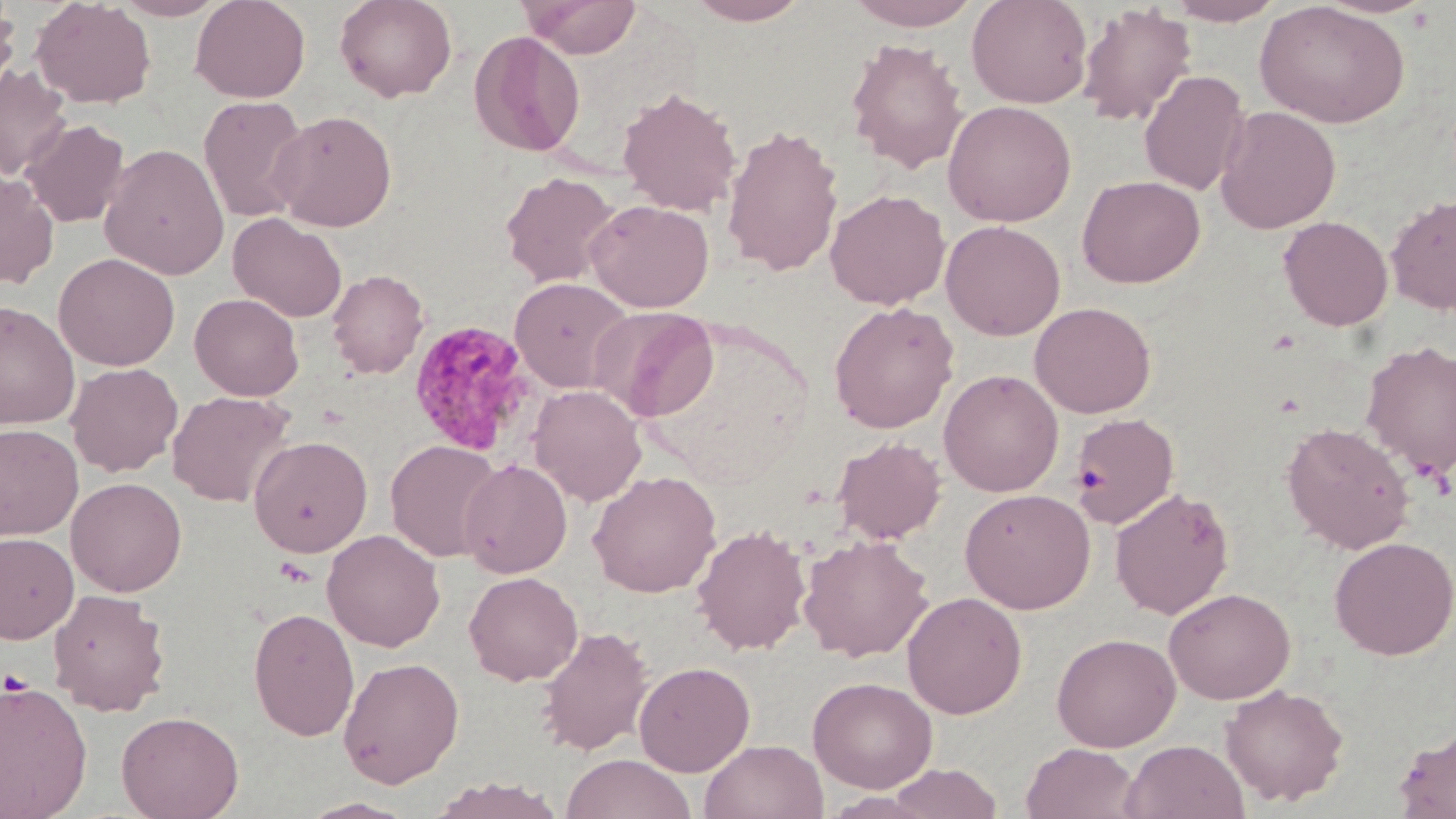
slide_level_diagnosis: Plasmodium malariae
field_of_view: single
platelet_locations: 'approximate bounding boxes as named x1/y1/x2/y2 corners in pixels: (x1=2, y1=668, x2=32, y2=696)'
plasmodium_malariae_infected_red_blood_cell_locations: 'approximate bounding boxes as named x1/y1/x2/y2 corners in pixels: (x1=408, y1=320, x2=534, y2=456)'
stain: May-Grünwald-Giemsa
magnification: 1000x
preparation: thin blood smear
image_size: 1456×819 pixels
modality: light microscopy
uninfected_red_blood_cell_locations: 'approximate bounding boxes as named x1/y1/x2/y2 corners in pixels: (x1=31, y1=0, x2=156, y2=109), (x1=114, y1=0, x2=227, y2=21), (x1=191, y1=0, x2=310, y2=102), (x1=334, y1=0, x2=457, y2=102), (x1=519, y1=0, x2=642, y2=58), (x1=684, y1=0, x2=814, y2=25), (x1=844, y1=0, x2=982, y2=30), (x1=966, y1=0, x2=1093, y2=109), (x1=1163, y1=0, x2=1286, y2=26), (x1=0, y1=2, x2=20, y2=103), (x1=1255, y1=2, x2=1411, y2=129), (x1=1075, y1=3, x2=1197, y2=127), (x1=469, y1=30, x2=586, y2=157), (x1=846, y1=37, x2=968, y2=175), (x1=0, y1=65, x2=73, y2=180), (x1=1138, y1=70, x2=1251, y2=196), (x1=617, y1=86, x2=741, y2=215), (x1=198, y1=95, x2=311, y2=222), (x1=942, y1=100, x2=1077, y2=227), (x1=1214, y1=106, x2=1341, y2=234), (x1=270, y1=110, x2=398, y2=232), (x1=22, y1=119, x2=129, y2=228), (x1=722, y1=122, x2=844, y2=278), (x1=99, y1=143, x2=230, y2=279), (x1=0, y1=170, x2=59, y2=288), (x1=500, y1=171, x2=620, y2=288), (x1=1076, y1=175, x2=1205, y2=288), (x1=825, y1=189, x2=950, y2=310), (x1=1385, y1=193, x2=1456, y2=314), (x1=585, y1=198, x2=715, y2=312), (x1=228, y1=213, x2=347, y2=322), (x1=1278, y1=215, x2=1393, y2=331), (x1=940, y1=220, x2=1066, y2=341), (x1=54, y1=253, x2=180, y2=371), (x1=326, y1=269, x2=429, y2=378), (x1=510, y1=277, x2=634, y2=393), (x1=189, y1=293, x2=304, y2=400), (x1=0, y1=301, x2=79, y2=429), (x1=828, y1=301, x2=959, y2=433), (x1=1030, y1=301, x2=1156, y2=418), (x1=592, y1=306, x2=719, y2=422), (x1=1361, y1=340, x2=1456, y2=479), (x1=66, y1=362, x2=183, y2=477), (x1=938, y1=369, x2=1063, y2=497), (x1=529, y1=384, x2=647, y2=506), (x1=167, y1=390, x2=295, y2=507), (x1=1070, y1=413, x2=1180, y2=529), (x1=1280, y1=421, x2=1416, y2=553), (x1=0, y1=423, x2=83, y2=540), (x1=248, y1=435, x2=373, y2=557), (x1=832, y1=436, x2=946, y2=544), (x1=386, y1=439, x2=504, y2=562), (x1=460, y1=459, x2=573, y2=578), (x1=587, y1=470, x2=722, y2=598), (x1=66, y1=477, x2=186, y2=597), (x1=960, y1=487, x2=1096, y2=614), (x1=1110, y1=487, x2=1235, y2=619), (x1=692, y1=524, x2=811, y2=655), (x1=322, y1=529, x2=445, y2=651), (x1=0, y1=532, x2=78, y2=644), (x1=799, y1=534, x2=934, y2=662), (x1=1329, y1=536, x2=1455, y2=660), (x1=464, y1=571, x2=583, y2=686), (x1=1164, y1=587, x2=1295, y2=704), (x1=48, y1=588, x2=170, y2=717), (x1=902, y1=591, x2=1027, y2=719), (x1=248, y1=607, x2=359, y2=741), (x1=536, y1=625, x2=654, y2=756), (x1=1051, y1=632, x2=1181, y2=751), (x1=338, y1=657, x2=464, y2=788), (x1=634, y1=661, x2=755, y2=777), (x1=807, y1=676, x2=938, y2=793), (x1=0, y1=678, x2=93, y2=817), (x1=1221, y1=683, x2=1349, y2=807), (x1=116, y1=710, x2=244, y2=819), (x1=1394, y1=727, x2=1456, y2=818), (x1=700, y1=738, x2=828, y2=819), (x1=1120, y1=739, x2=1250, y2=819), (x1=1021, y1=743, x2=1139, y2=819), (x1=561, y1=752, x2=695, y2=819), (x1=885, y1=762, x2=1003, y2=818), (x1=429, y1=776, x2=565, y2=819), (x1=297, y1=796, x2=419, y2=818)'